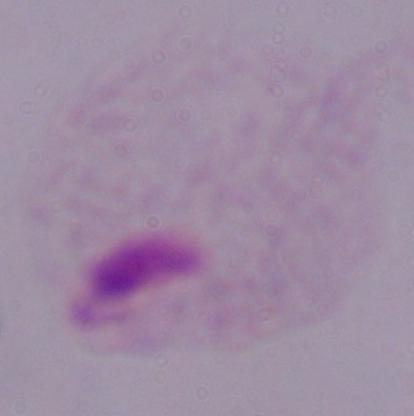

{
  "magnification": "1000x",
  "modality": "micrograph",
  "identification": "trichomonad"
}